Outline each Plasmodium malariae-infected red blood cell.
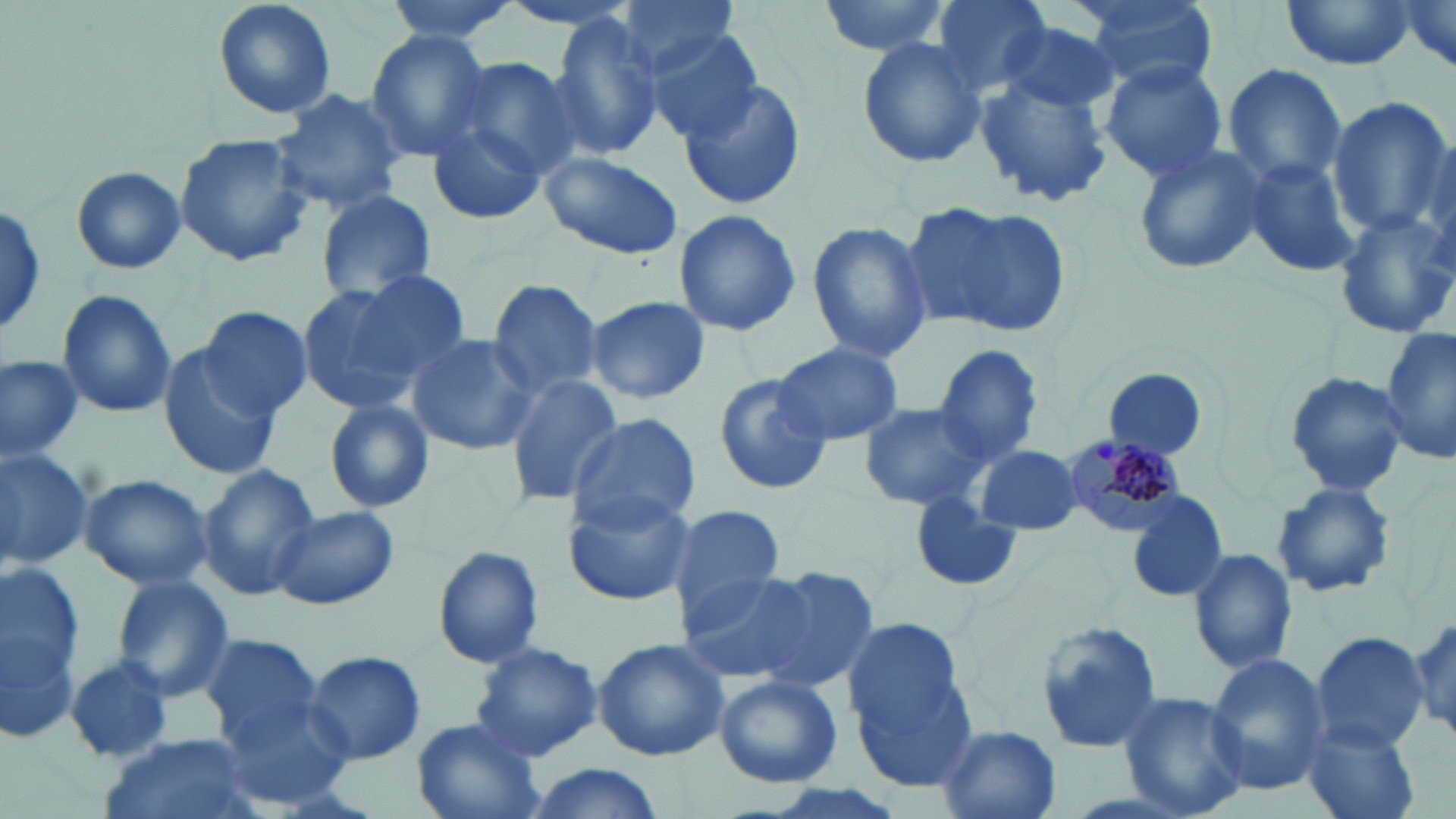
Approximate bounding boxes as (x1, y1, x2, y2) in pixels.
Plasmodium malariae-infected red blood cells: (1061, 435, 1189, 539).

Uninfected red blood cell locations: (212, 0, 337, 121), (383, 0, 521, 44), (500, 0, 641, 36), (618, 0, 744, 78), (815, 0, 953, 57), (928, 0, 1057, 96), (1076, 0, 1217, 91), (1280, 0, 1417, 71), (1386, 1, 1456, 79), (546, 15, 666, 164), (998, 18, 1122, 117), (643, 29, 766, 145), (365, 31, 490, 159), (856, 34, 990, 170), (450, 56, 584, 177), (1098, 58, 1231, 183), (1222, 64, 1348, 190), (975, 75, 1113, 207), (678, 76, 807, 211), (270, 89, 408, 214), (1328, 97, 1450, 239), (426, 115, 544, 228), (174, 131, 312, 270), (1131, 140, 1270, 277), (539, 149, 685, 262), (1240, 155, 1362, 279), (71, 167, 187, 275), (313, 190, 437, 305), (904, 199, 1070, 339), (0, 204, 48, 339), (671, 209, 801, 338), (1332, 209, 1456, 339), (805, 220, 933, 363), (354, 262, 475, 372), (484, 278, 605, 401), (293, 284, 427, 414), (55, 289, 177, 419), (584, 295, 711, 405), (197, 306, 313, 418), (1381, 329, 1455, 468), (406, 333, 541, 456), (772, 340, 903, 446), (157, 341, 287, 482), (933, 344, 1045, 466), (0, 354, 83, 463), (1102, 367, 1210, 463), (1282, 370, 1409, 499), (505, 373, 623, 504), (713, 373, 834, 496), (322, 398, 436, 514), (858, 400, 992, 512), (567, 411, 699, 531), (974, 443, 1083, 537), (0, 445, 94, 571), (197, 462, 320, 600), (80, 473, 214, 590), (1271, 481, 1396, 599), (560, 486, 696, 606), (1125, 489, 1230, 604), (909, 491, 1022, 590), (267, 505, 400, 610), (666, 505, 789, 625), (431, 544, 545, 668), (1188, 547, 1299, 675), (0, 560, 85, 738), (751, 564, 879, 693), (678, 570, 815, 685), (111, 574, 235, 700), (1410, 610, 1454, 744), (1035, 621, 1165, 756), (843, 622, 978, 787), (200, 631, 323, 745), (1311, 632, 1430, 754), (591, 638, 731, 760), (469, 643, 603, 762), (301, 650, 427, 766), (1203, 652, 1328, 795), (66, 654, 176, 762), (714, 673, 843, 788), (213, 689, 355, 810), (1118, 690, 1252, 817), (409, 717, 547, 819), (1300, 719, 1420, 819), (936, 725, 1062, 819), (98, 737, 257, 819), (523, 764, 668, 819). Slide-level diagnosis: Plasmodium malariae. Image is 1456×819 pixels. Thin blood smear. Single field of view. May-Grünwald-Giemsa stain. 1000x magnification. Optical microscopy.